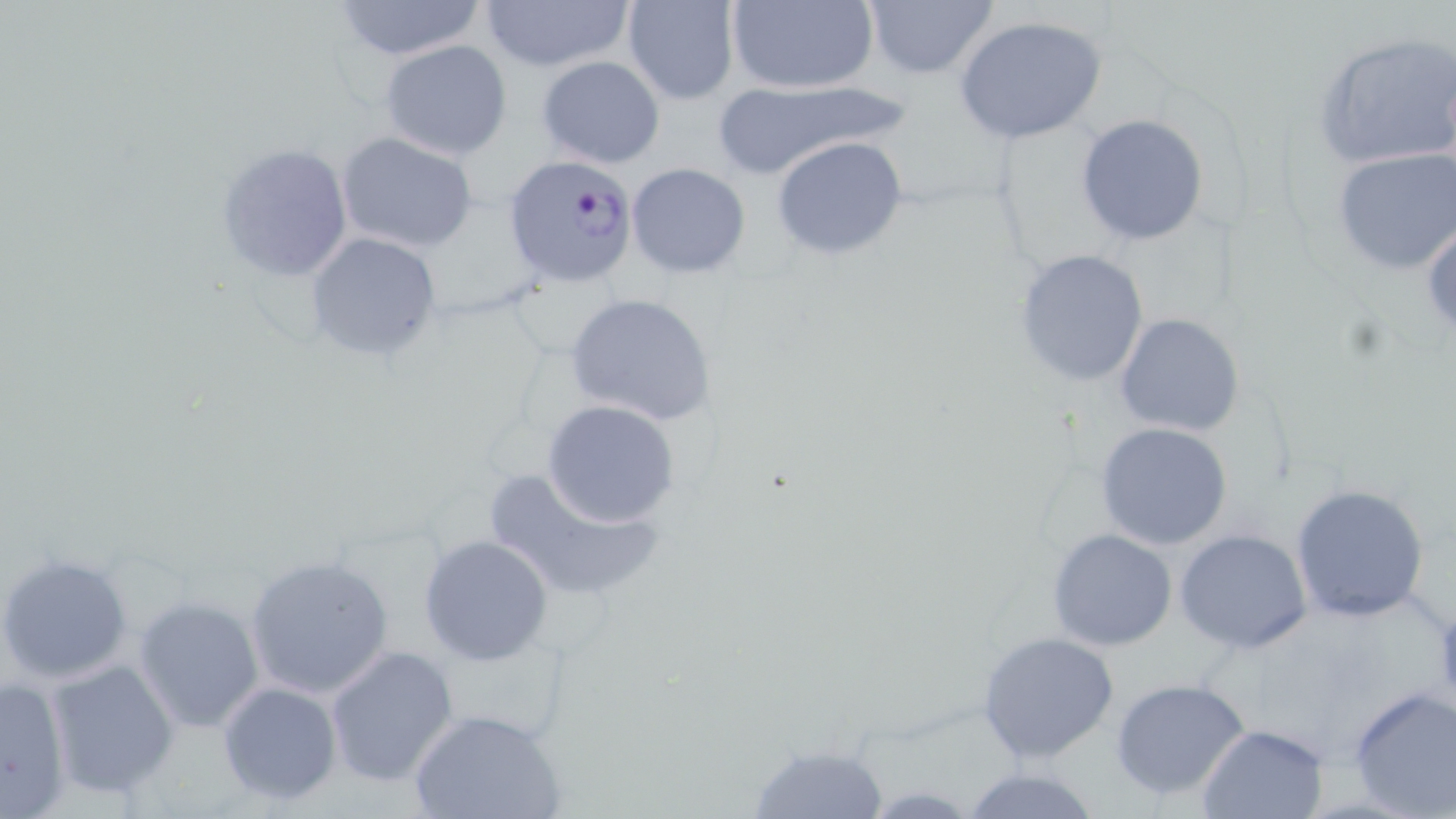 Approximate bounding boxes as (x1,y1)-(x2,y2) corner pairs in pixels. Plasmodium falciparum-infected red blood cell locations: (505,154)-(641,285). Uninfected red blood cell locations: (330,0)-(487,61), (621,0)-(742,105), (725,0)-(880,96), (478,1)-(636,74), (861,1)-(1000,82), (954,15)-(1108,145), (1311,30)-(1456,172), (377,39)-(514,158), (536,55)-(666,170), (710,80)-(910,181), (1075,114)-(1211,247), (334,132)-(480,255), (770,134)-(908,262), (217,141)-(354,285), (1332,147)-(1456,274), (626,163)-(750,279), (1423,218)-(1456,338), (305,233)-(442,360), (1013,248)-(1149,388), (566,293)-(717,428), (1115,312)-(1244,437), (540,400)-(679,528), (1095,422)-(1236,552), (483,468)-(664,604), (1288,484)-(1431,623), (1046,528)-(1178,651), (1173,528)-(1315,655), (417,533)-(554,666), (0,552)-(134,686), (245,555)-(394,699), (1431,595)-(1456,711), (135,596)-(265,733), (975,630)-(1121,764), (324,645)-(458,786), (46,660)-(179,799), (0,675)-(71,815), (1110,677)-(1252,802), (217,680)-(343,806), (1347,686)-(1456,817), (409,706)-(564,819), (1196,723)-(1329,819), (746,742)-(890,817), (960,763)-(1103,819). Slide-level diagnosis: Plasmodium falciparum. Thin blood film. 1000x magnification. Single field of view. Optical microscopy. May-Grünwald-Giemsa stain. Image is 1456×819 pixels.